Identify the cell.
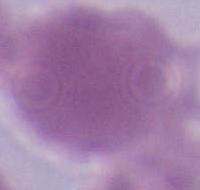

An erythrocyte.

Summary:
  - Magnification: 1000x
  - Modality: micrograph